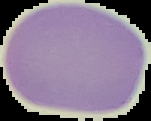
preparation = thin blood film
image size = 151×121 pixels
image type = segmented cell region with the area outside set to black
result = negative for malaria parasites